Comment on the morphology of the red blood cells.
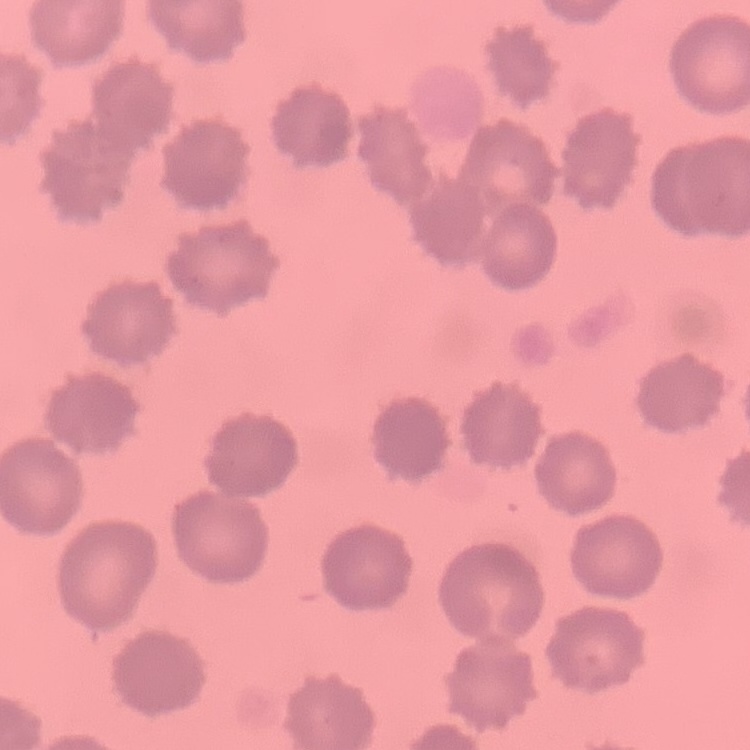
They show no rouleaux formation.

Thin blood film. One tile cut from a larger photomicrograph. Stained with either Field's or Giemsa.